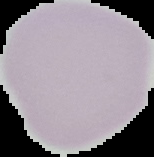
malaria status = uninfected
image type = cell region segmented out of the field of view; surrounding area masked to black
preparation = thin blood film
image size = 154×157 pixels